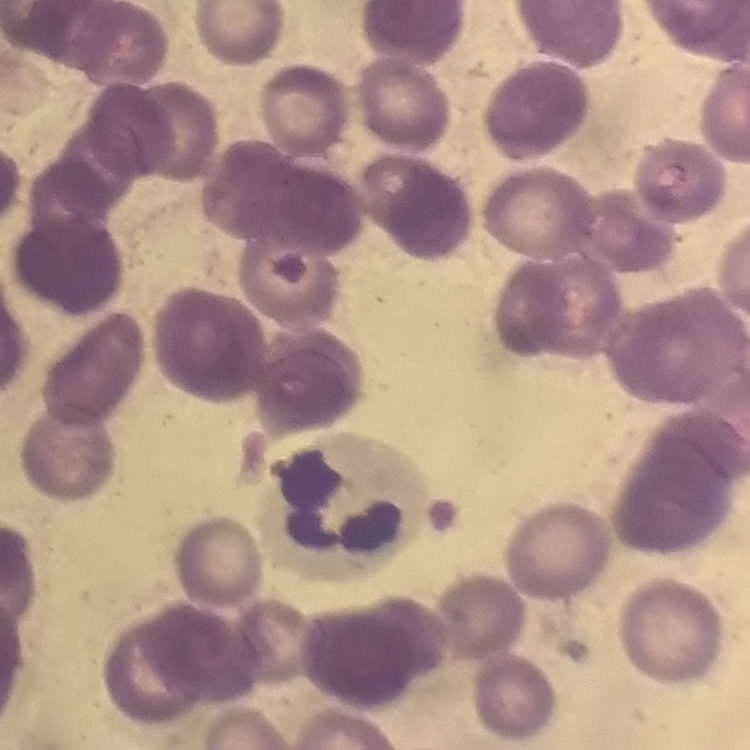
Summary:
  - Red blood cell morphology: rouleaux formation
  - Preparation: thin blood film
  - Image type: square crop of a larger photomicrograph
  - Stain: Field's or Giemsa